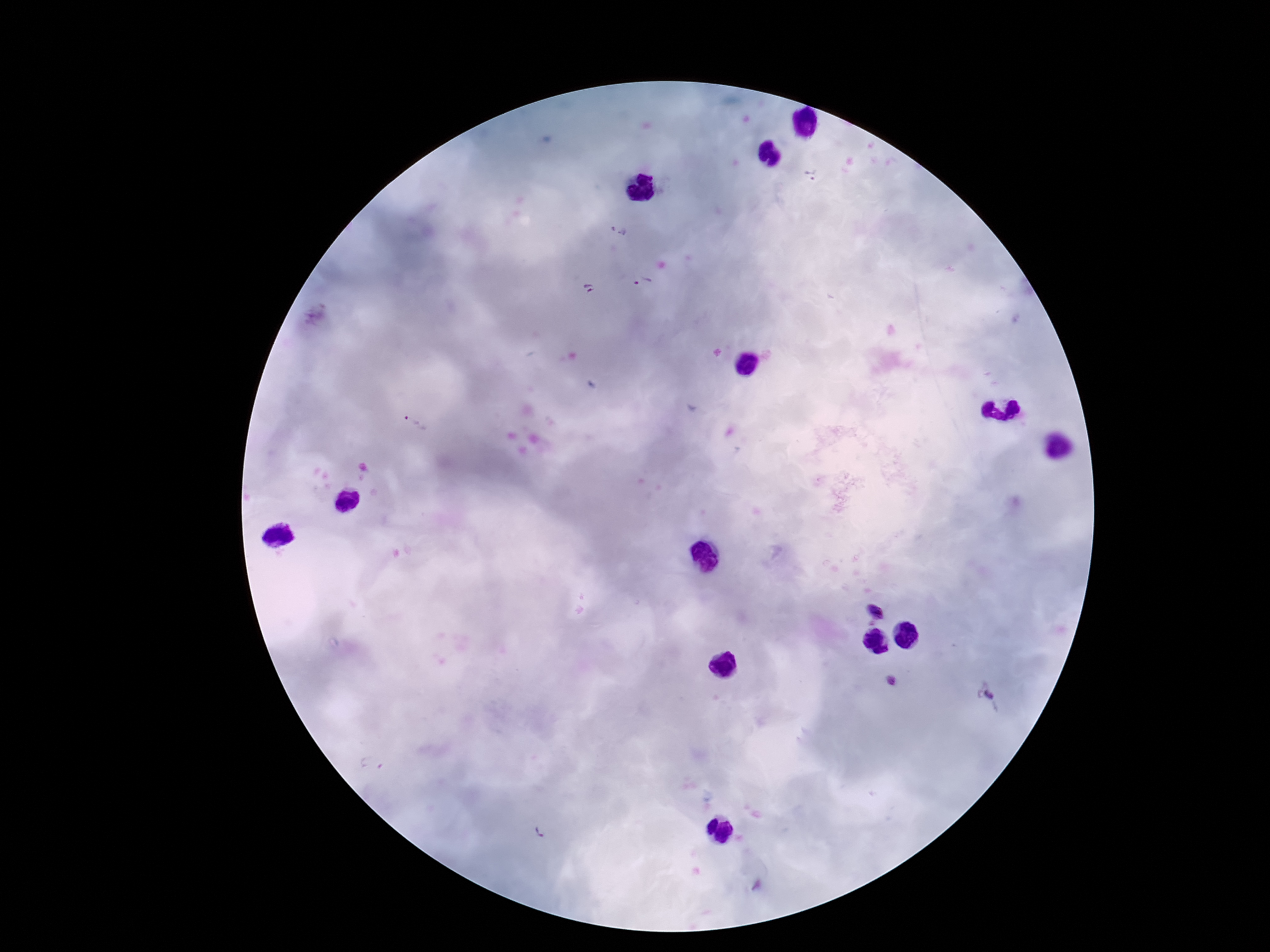
Approximate centers as [x, y] in pixels. Plasmodium parasite locations: [811, 172], [617, 232], [643, 281], [589, 289], [316, 314], [417, 420], [876, 612], [891, 682], [987, 692], [372, 764], [540, 831]. Smartphone photograph taken through the microscope eyepiece. Thick blood film. Image is 1270×952 pixels. 100x magnification. Patient malaria status: infected. Giemsa-stained preparation. Single field of view.